Locate every uninfected red blood cell.
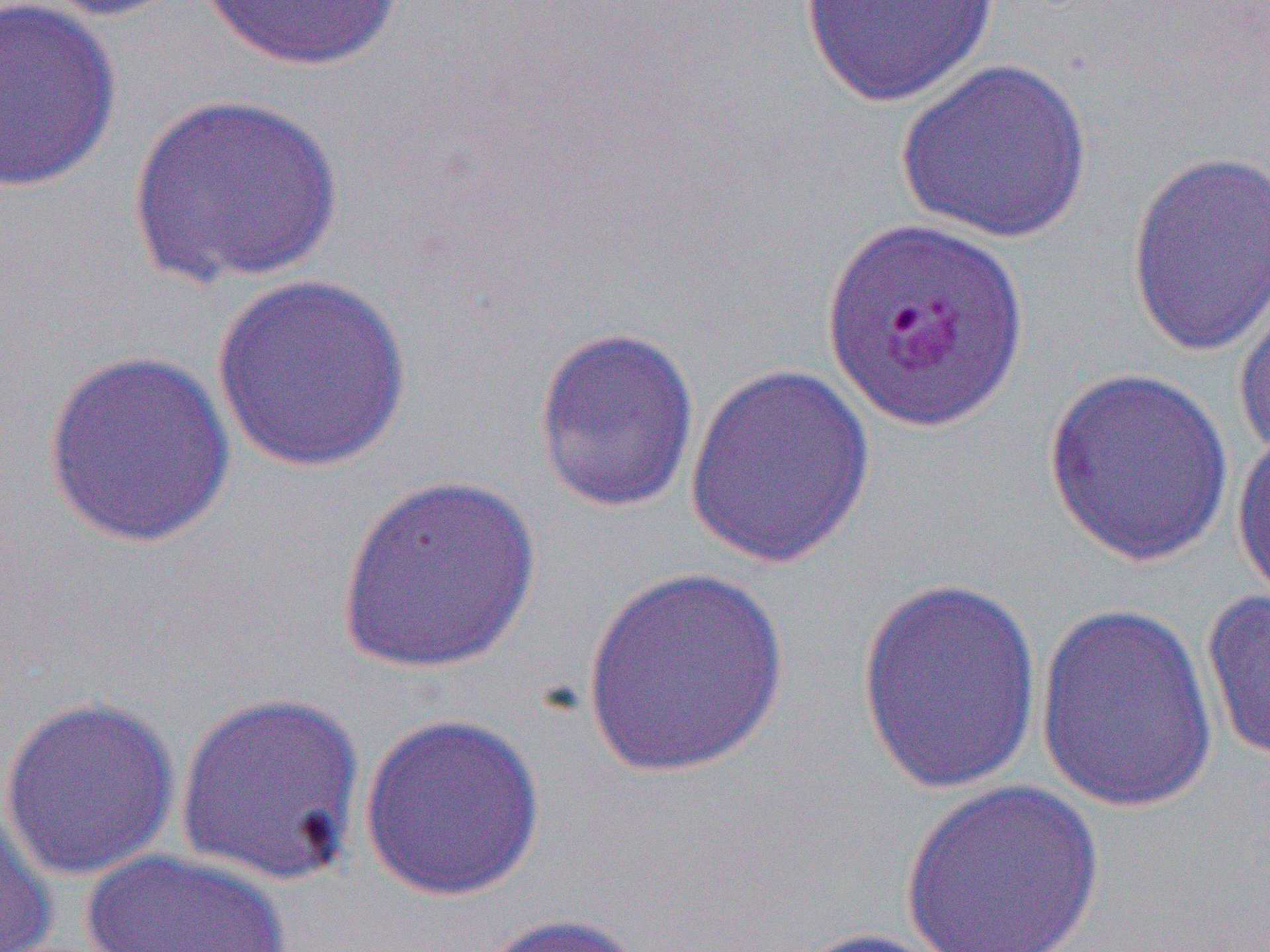

Approximate bounding boxes as [x1, y1, x2, y2] in pixels.
Uninfected red blood cells: [1, 0, 122, 193], [31, 0, 199, 23], [198, 0, 408, 72], [799, 0, 1000, 107], [895, 58, 1093, 244], [129, 92, 342, 289], [1126, 148, 1270, 361], [210, 273, 413, 474], [1232, 277, 1270, 463], [532, 325, 701, 515], [41, 349, 237, 550], [683, 364, 877, 572], [1043, 367, 1235, 567], [1232, 425, 1270, 606], [334, 473, 542, 677], [580, 565, 792, 782], [856, 576, 1043, 794], [1200, 587, 1270, 766], [1033, 600, 1218, 815], [173, 690, 368, 887], [0, 694, 181, 882], [357, 712, 545, 902], [899, 778, 1106, 951], [0, 800, 58, 952], [79, 849, 296, 952], [469, 912, 649, 952], [782, 926, 958, 952].

slide-level diagnosis = Plasmodium falciparum
field of view = one of a larger specimen
image size = 1270×952 pixels
modality = light microscopy
preparation = thin blood smear
magnification = 1000x